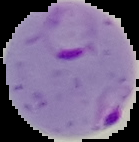 From a thin blood film. Image is 139×142 pixels. The area outside the segmented cell region is set to black. Result: Plasmodium parasites identified.